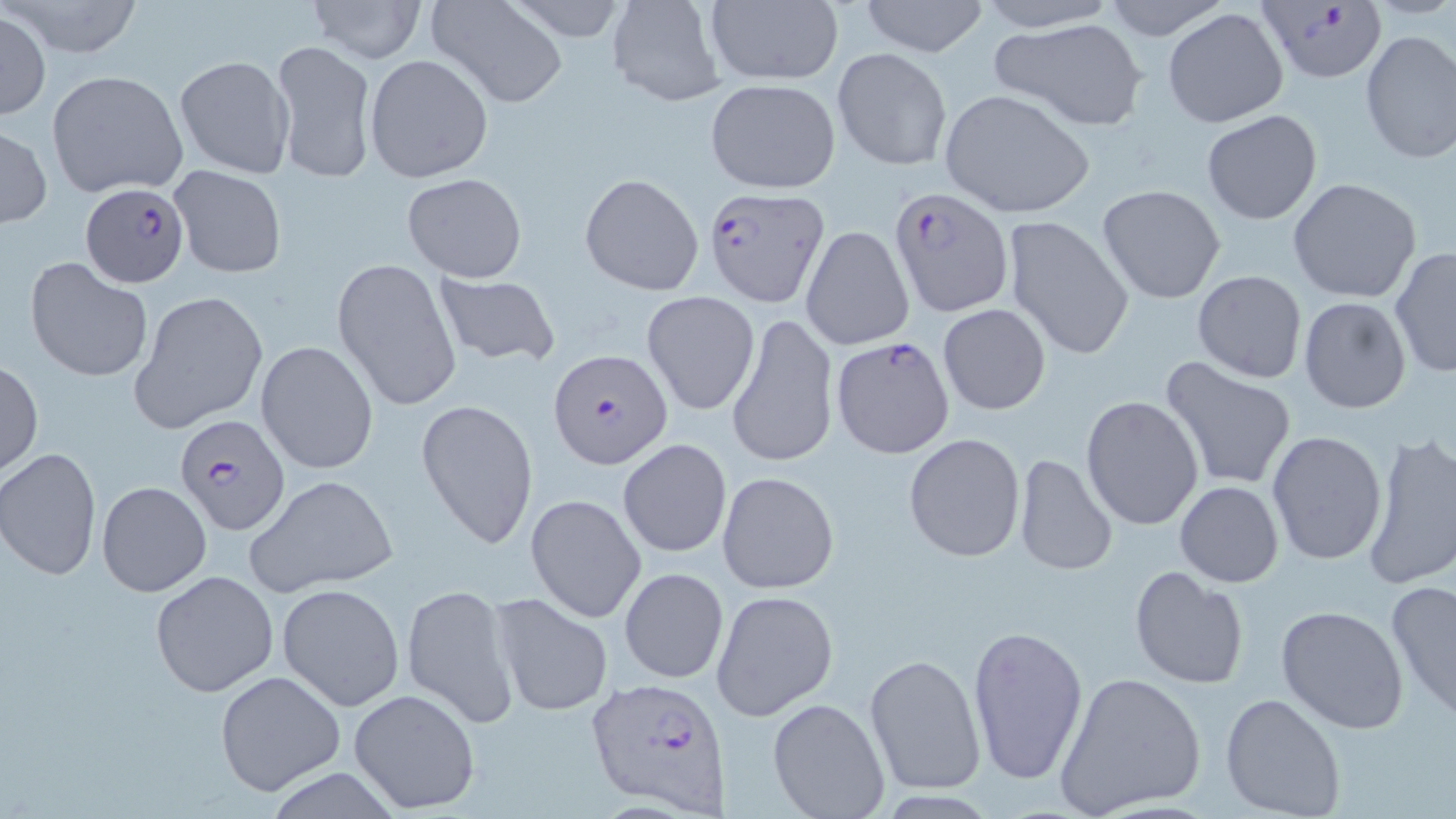
{
  "slide_level_diagnosis": "Plasmodium falciparum",
  "modality": "light microscopy",
  "preparation": "thin blood film",
  "uninfected_red_blood_cell_locations_subset": "approximate bounding boxes as (x1, y1, x2, y2) in pixels: (8, 0, 147, 59), (304, 0, 426, 64), (427, 0, 569, 108), (607, 0, 727, 107), (704, 0, 845, 87), (856, 0, 993, 57), (969, 0, 1122, 32), (1098, 0, 1234, 41), (1161, 8, 1290, 128), (1, 11, 49, 121), (987, 15, 1150, 132), (1359, 30, 1456, 164), (268, 39, 377, 185), (832, 47, 952, 171), (364, 53, 494, 183), (173, 55, 294, 178), (46, 69, 187, 198), (704, 79, 842, 192), (938, 89, 1095, 218), (1201, 109, 1323, 226), (0, 126, 51, 229), (169, 165, 287, 277), (402, 173, 529, 281), (579, 173, 704, 296), (1288, 176, 1423, 303), (1097, 183, 1227, 305), (1003, 217, 1133, 362), (801, 225, 914, 351), (1388, 245, 1456, 381), (25, 259, 153, 383), (332, 259, 461, 413), (1192, 270, 1307, 384), (434, 271, 561, 368), (129, 290, 269, 437), (642, 292, 759, 414), (1297, 296, 1413, 415), (938, 303, 1052, 415), (727, 313, 838, 468), (830, 337, 957, 459), (255, 340, 379, 476), (1159, 357, 1297, 493), (0, 358, 43, 477), (1080, 395, 1204, 530), (416, 397, 539, 552), (1266, 431, 1389, 566), (1360, 431, 1456, 592), (903, 432, 1027, 562), (618, 437, 732, 559), (0, 448, 102, 581), (1012, 453, 1118, 575), (719, 470, 838, 595), (245, 473, 398, 598), (96, 480, 212, 597), (1174, 481, 1286, 587), (525, 492, 647, 624), (1129, 566, 1249, 689), (619, 567, 729, 683), (149, 570, 279, 699), (1384, 578, 1456, 721), (276, 583, 405, 711), (404, 583, 523, 731), (711, 589, 838, 720), (491, 593, 614, 717), (1275, 604, 1410, 735), (966, 623, 1088, 784), (864, 653, 985, 794), (215, 669, 346, 795), (1054, 671, 1208, 817), (348, 687, 481, 814), (1221, 693, 1347, 818), (767, 698, 891, 819)",
  "image_size": "1456×819 pixels",
  "plasmodium_falciparum_infected_red_blood_cell_locations_subset": "approximate bounding boxes as (x1, y1, x2, y2) in pixels: (1253, 2, 1387, 85), (80, 181, 191, 289), (702, 187, 830, 308), (547, 348, 674, 468), (173, 416, 291, 537), (588, 676, 728, 814)",
  "stain": "May-Grünwald-Giemsa",
  "magnification": "1000x",
  "field_of_view": "single"
}